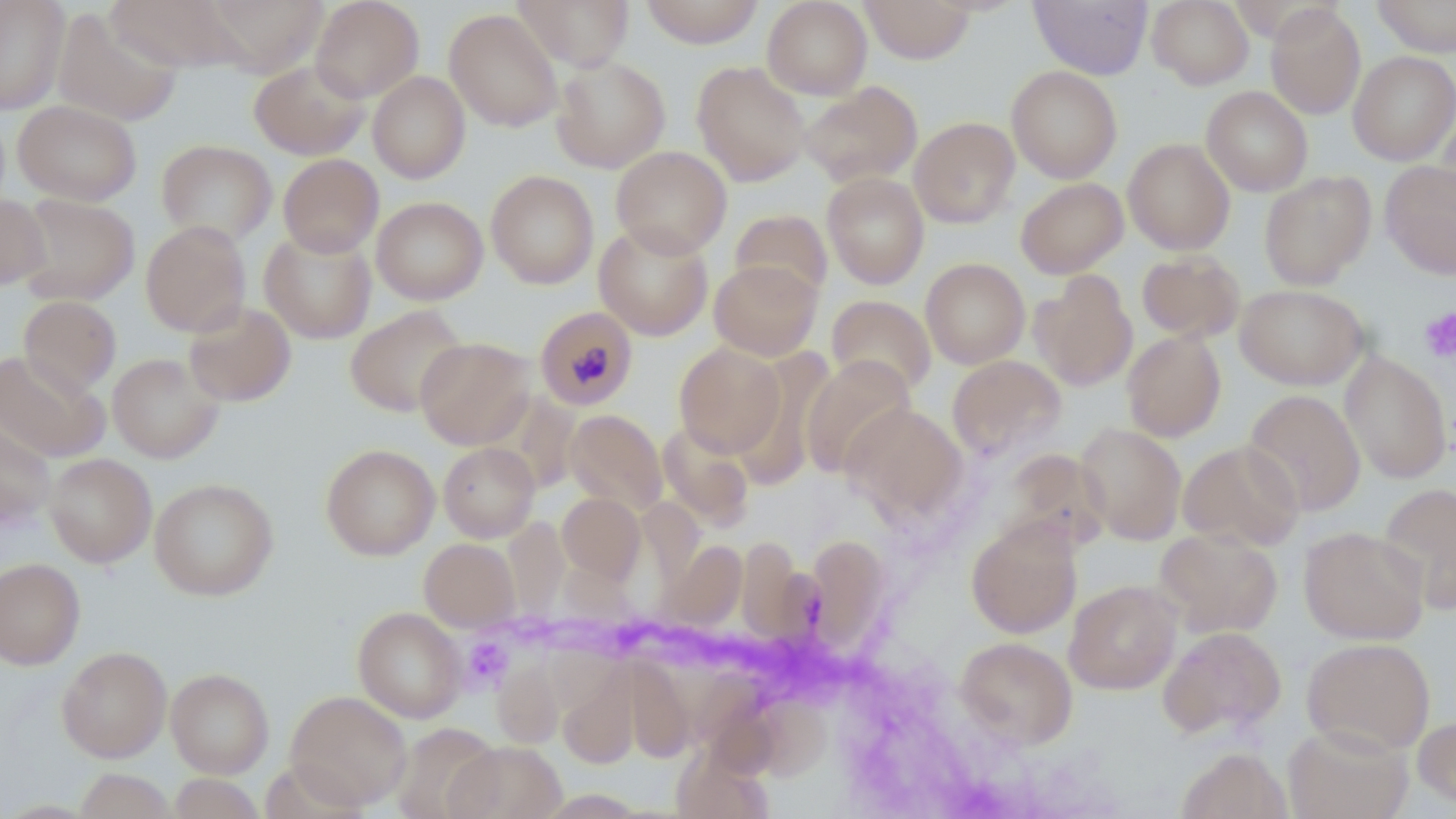
Summary:
  - Coordinate format: approximate bounding boxes as (x1,y1)-(x2,y2) corner pairs in pixels
  - Plasmodium malariae-infected red blood cell locations: (535,305)-(639,411)
  - Platelet locations: (1419,307)-(1456,362), (462,636)-(511,690)
  - Uninfected red blood cell locations: (0,0)-(70,114), (105,0)-(241,71), (202,0)-(329,76), (310,0)-(424,102), (513,0)-(634,71), (640,0)-(765,48), (762,0)-(873,99), (860,0)-(975,64), (1029,0)-(1152,80), (1147,0)-(1254,89), (1371,0)-(1456,57), (1265,3)-(1366,119), (51,7)-(184,127), (443,8)-(563,132), (1348,50)-(1456,165), (551,55)-(671,173), (249,59)-(370,160), (692,61)-(812,186), (1006,66)-(1122,183), (368,71)-(470,183), (799,81)-(923,188), (1201,86)-(1313,196), (13,99)-(142,206), (1435,108)-(1456,224), (909,117)-(1020,228), (1123,137)-(1235,254), (156,139)-(278,247), (611,146)-(731,258), (278,154)-(384,257), (1380,161)-(1456,279), (485,170)-(599,289), (822,171)-(930,289), (1259,171)-(1375,290), (1015,177)-(1128,278), (0,193)-(49,290), (14,193)-(139,306), (371,196)-(488,304), (729,209)-(833,303), (140,220)-(251,337), (594,221)-(713,340), (259,228)-(376,344), (1137,251)-(1245,343), (920,257)-(1030,369), (709,258)-(822,361), (1030,271)-(1138,391), (1235,284)-(1369,390), (19,295)-(121,396), (826,295)-(937,396), (183,300)-(296,406), (345,305)-(468,417), (1122,330)-(1226,442), (415,336)-(536,450), (674,343)-(786,457), (730,348)-(835,488), (0,350)-(110,462), (1339,351)-(1452,484), (107,353)-(223,463), (947,355)-(1066,460), (800,356)-(916,478), (1243,389)-(1366,516), (841,403)-(969,525), (565,409)-(668,515), (657,420)-(755,530), (0,421)-(56,529), (1075,422)-(1187,544), (1178,439)-(1305,552), (438,441)-(540,542), (320,444)-(440,560), (999,448)-(1110,552), (44,453)-(157,567), (149,478)-(279,600), (1377,482)-(1456,615), (558,492)-(645,584), (503,516)-(569,621), (966,516)-(1083,638), (1299,526)-(1430,645), (1154,527)-(1283,638), (804,536)-(891,652), (419,538)-(520,630), (658,539)-(746,632), (736,540)-(806,642), (0,558)-(85,670), (1064,579)-(1181,695), (352,606)-(467,722), (1158,625)-(1286,739), (955,636)-(1078,749), (1302,637)-(1436,755), (57,646)-(171,762), (491,656)-(566,749), (615,660)-(700,764), (166,667)-(274,778), (558,671)-(640,769), (285,690)-(412,810), (747,694)-(831,780), (1413,714)-(1456,809), (391,723)-(501,818), (1283,723)-(1412,819), (446,741)-(566,819), (674,744)-(773,819), (1176,747)-(1293,819), (75,769)-(176,818), (169,773)-(266,818)
  - Slide-level diagnosis: Plasmodium malariae
  - Stain: May-Grünwald-Giemsa
  - Magnification: 1000x
  - Preparation: thin blood film
  - Image size: 1456×819 pixels
  - Field of view: single
  - Modality: optical microscopy